Classify this cell by malaria status.
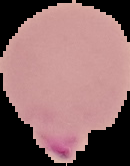
Parasitized.

Summary:
  - Image type: cell region segmented out of the field of view; surrounding area masked to black
  - Preparation: thin blood film
  - Image size: 130×166 pixels